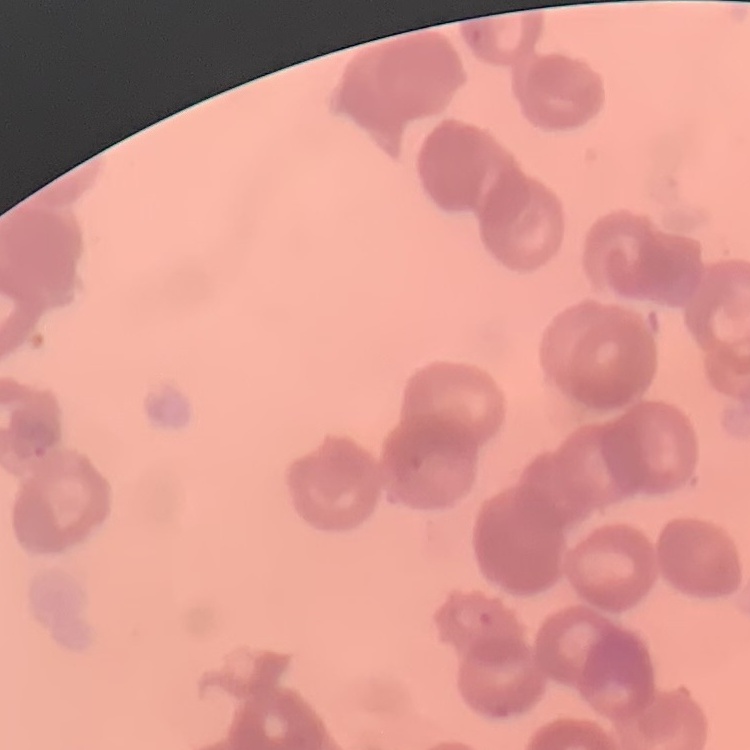

Summary:
  - Red blood cell morphology: rouleaux formation
  - Preparation: thin peripheral smear
  - Stain: Field's or Giemsa
  - Image type: one tile cut from a larger photomicrograph